State the blood parasite species.
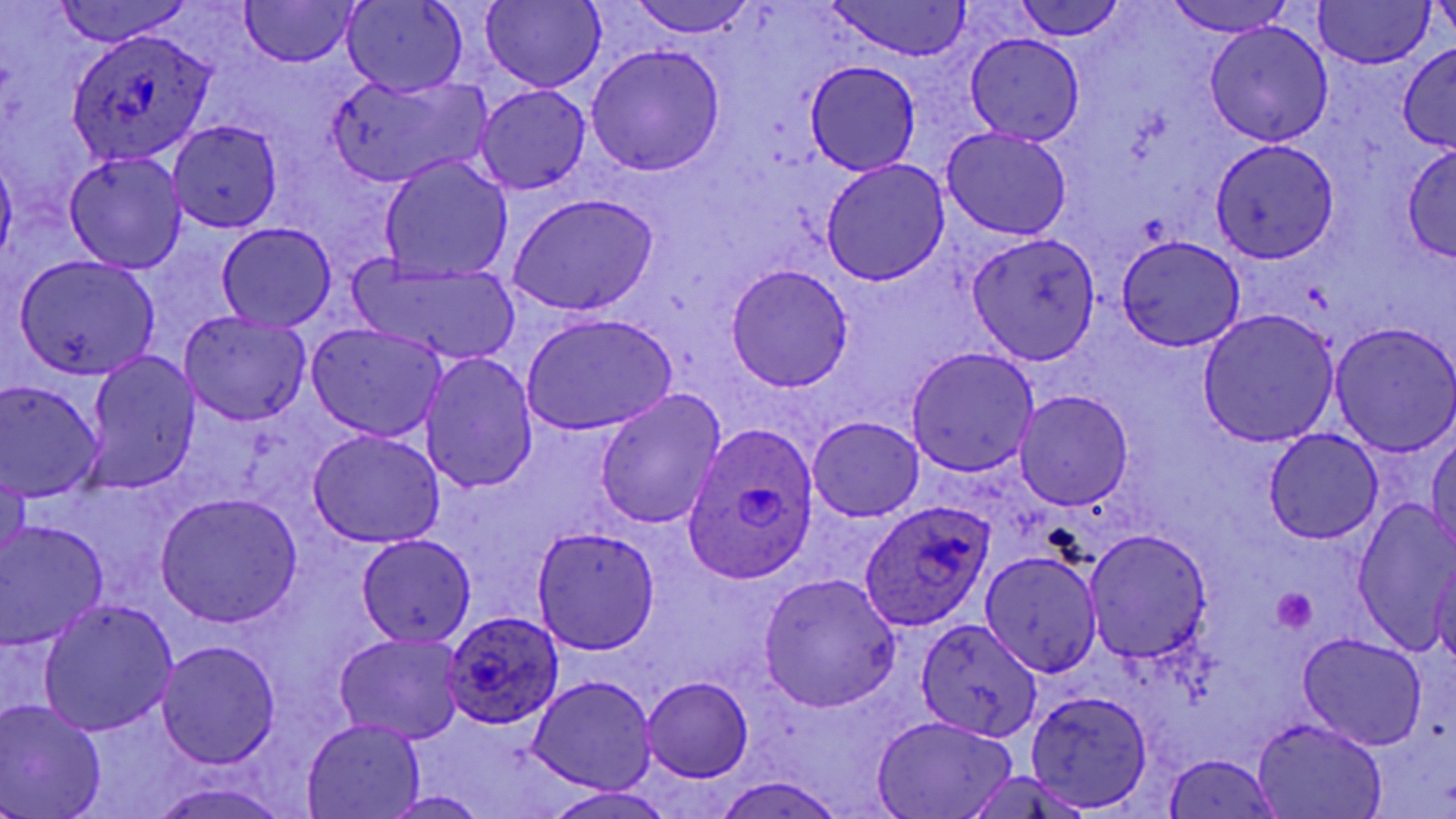
Plasmodium ovale.

Approximate bounding boxes as (x1, y1, x2, y2) in pixels. Plasmodium ovale-infected red blood cell locations: (65, 28, 217, 165), (686, 421, 822, 582), (862, 498, 993, 632), (443, 612, 565, 727). Platelet locations: (1273, 588, 1317, 633). Uninfected red blood cell locations: (52, 0, 190, 47), (241, 0, 356, 68), (342, 0, 468, 98), (624, 0, 761, 36), (826, 0, 973, 61), (1162, 0, 1294, 36), (482, 1, 604, 92), (1312, 1, 1435, 69), (1431, 1, 1455, 44), (1014, 2, 1121, 41), (1205, 20, 1333, 147), (964, 33, 1085, 146), (1397, 42, 1456, 152), (587, 44, 725, 176), (806, 61, 921, 175), (328, 75, 488, 188), (475, 84, 590, 195), (166, 120, 283, 234), (942, 127, 1073, 240), (1210, 139, 1338, 263), (1402, 145, 1456, 261), (0, 152, 17, 270), (63, 152, 188, 273), (379, 155, 514, 285), (821, 158, 951, 286), (507, 193, 660, 316), (217, 222, 336, 332), (966, 232, 1101, 363), (1116, 235, 1244, 352), (15, 254, 156, 379), (351, 254, 519, 367), (725, 263, 855, 391), (1197, 310, 1339, 447), (179, 311, 312, 426), (522, 313, 677, 436), (1329, 321, 1456, 454), (305, 323, 448, 442), (906, 347, 1039, 476), (420, 351, 538, 494), (83, 353, 199, 493), (0, 381, 103, 500), (595, 389, 727, 531), (1015, 390, 1134, 512), (809, 417, 923, 521), (1263, 428, 1383, 544), (308, 431, 443, 548), (1428, 431, 1456, 553), (0, 465, 29, 573), (156, 493, 303, 629), (1352, 501, 1456, 652), (0, 522, 108, 648), (531, 526, 660, 654), (1084, 529, 1213, 664), (356, 535, 477, 647), (980, 549, 1103, 676), (1430, 559, 1456, 668), (758, 573, 900, 711), (40, 601, 179, 735), (914, 618, 1041, 741), (335, 633, 467, 746), (1298, 634, 1427, 751), (156, 640, 282, 769), (528, 675, 658, 794), (642, 677, 752, 781), (1026, 689, 1154, 811), (0, 700, 107, 819), (871, 715, 1017, 819), (302, 717, 423, 819), (1252, 718, 1389, 819), (1161, 753, 1285, 819), (960, 770, 1097, 819), (716, 775, 845, 819), (147, 780, 294, 819), (541, 788, 682, 818), (381, 791, 485, 818). Captured at 1000x magnification. Image is 1456×819 pixels. May-Grünwald-Giemsa-stained preparation. Light microscopy. One field of a larger specimen. Thin blood film.